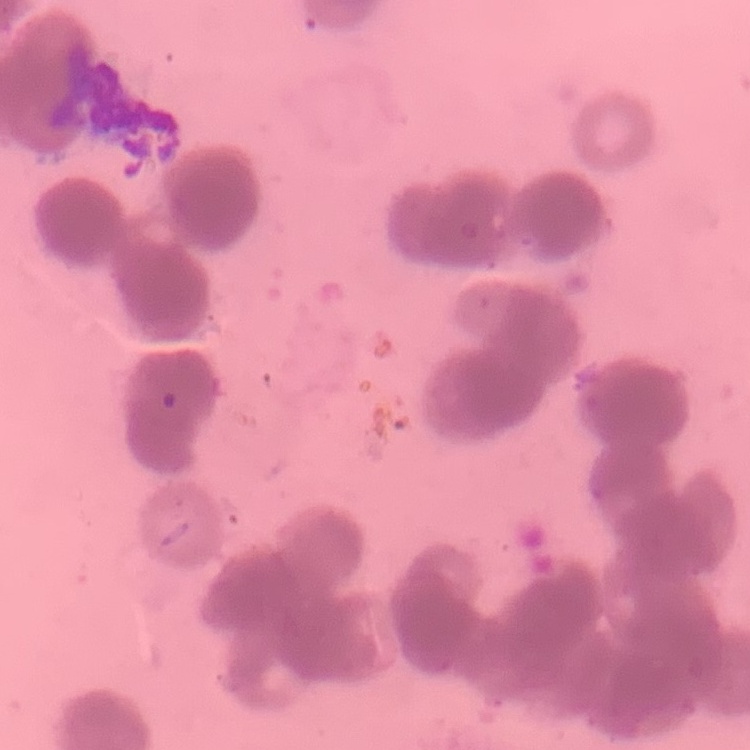

erythrocyte morphology = rouleaux formation
preparation = thin peripheral smear
image type = square crop of a larger photomicrograph
stain = Field's or Giemsa